State which parasite is depicted.
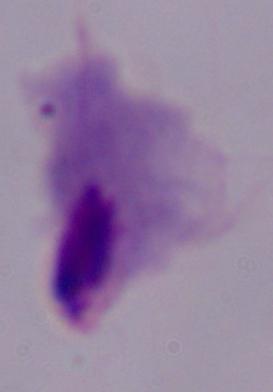
A trichomonad.

magnification = 1000x
modality = micrograph